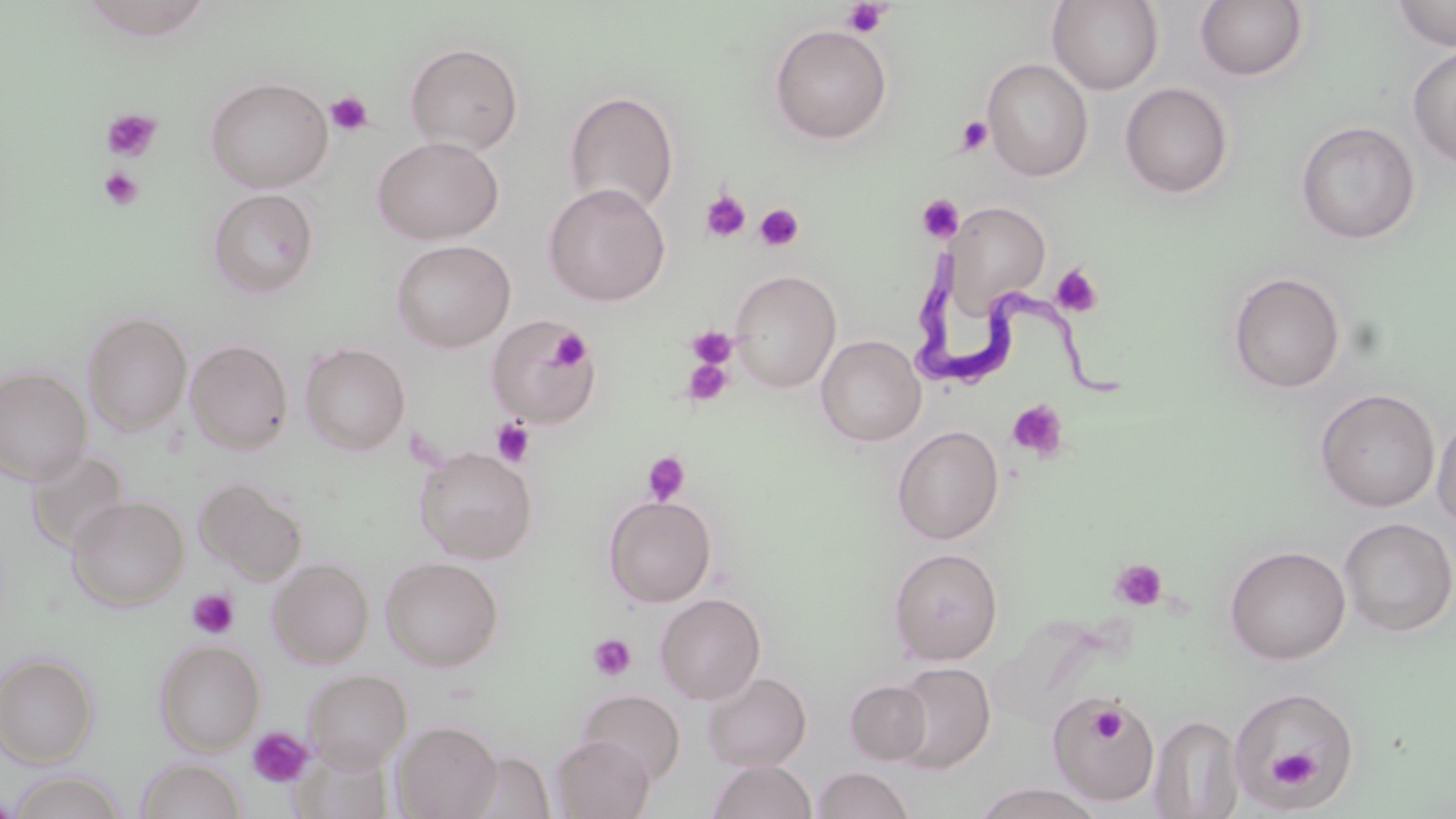

slide-level diagnosis = Trypanosoma brucei
field of view = single
magnification = 1000x
modality = light microscopy
preparation = thin blood smear
platelet locations = approximate bounding boxes as (x1, y1, x2, y2) in pixels: (840, 1, 892, 38), (326, 91, 373, 135), (100, 108, 162, 162), (955, 115, 995, 155), (98, 167, 144, 212), (701, 189, 752, 244), (917, 194, 964, 243), (754, 202, 805, 252), (1049, 264, 1103, 319), (686, 325, 738, 369), (549, 328, 590, 371), (682, 356, 734, 407), (1007, 399, 1069, 462), (491, 418, 535, 468), (642, 451, 690, 505), (1110, 558, 1168, 611), (186, 588, 239, 639), (587, 634, 636, 682), (1087, 701, 1129, 746), (247, 727, 314, 788), (1269, 748, 1319, 789)
stain = May-Grünwald-Giemsa
Trypanosoma brucei locations = approximate bounding boxes as (x1, y1, x2, y2) in pixels: (909, 244, 1141, 410)
uninfected red blood cell locations = approximate bounding boxes as (x1, y1, x2, y2) in pixels: (1047, 0, 1163, 94), (1195, 0, 1308, 82), (1390, 1, 1456, 50), (769, 24, 893, 144), (405, 42, 523, 156), (1407, 45, 1456, 168), (982, 59, 1093, 180), (205, 76, 333, 192), (1119, 82, 1234, 199), (563, 90, 680, 216), (1296, 121, 1419, 245), (372, 135, 504, 244), (543, 182, 671, 306), (207, 188, 319, 298), (947, 202, 1052, 311), (391, 239, 516, 352), (730, 270, 842, 392), (1227, 271, 1346, 393), (82, 311, 192, 434), (486, 315, 600, 429), (816, 335, 926, 446), (186, 339, 294, 454), (300, 343, 411, 455), (0, 366, 92, 483), (1315, 388, 1440, 513), (1432, 408, 1456, 532), (892, 424, 1004, 544), (414, 446, 538, 563), (24, 447, 130, 555), (195, 477, 309, 584), (67, 495, 189, 610), (603, 495, 717, 607), (1338, 517, 1455, 637), (1224, 545, 1351, 664), (887, 547, 1004, 665), (380, 556, 504, 672), (268, 557, 374, 668), (655, 592, 766, 705), (154, 639, 265, 756), (0, 652, 99, 766), (891, 661, 995, 774), (303, 670, 412, 771), (701, 671, 811, 771), (845, 680, 933, 764), (1228, 686, 1359, 808), (577, 689, 686, 785), (1048, 697, 1161, 807), (1148, 713, 1245, 818), (391, 720, 502, 818), (551, 734, 655, 818), (460, 751, 555, 818), (135, 758, 246, 818), (707, 759, 816, 818), (813, 766, 916, 819), (6, 770, 129, 819), (975, 783, 1102, 819), (0, 791, 19, 818)
image size = 1456×819 pixels